Report the malaria status of this cell.
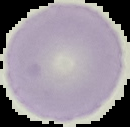
It is uninfected.

Image is 130×127 pixels. The area outside the segmented cell region is set to black. From a thin blood smear.